Name the cell type shown.
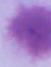
An erythrocyte.

modality = micrograph
magnification = 1000x